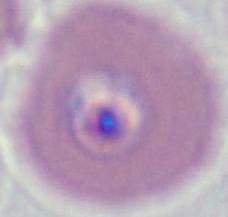
Micrograph. 400x or 1000x magnification. A Plasmodium parasite is shown.